Outline each blood parasite and name the species.
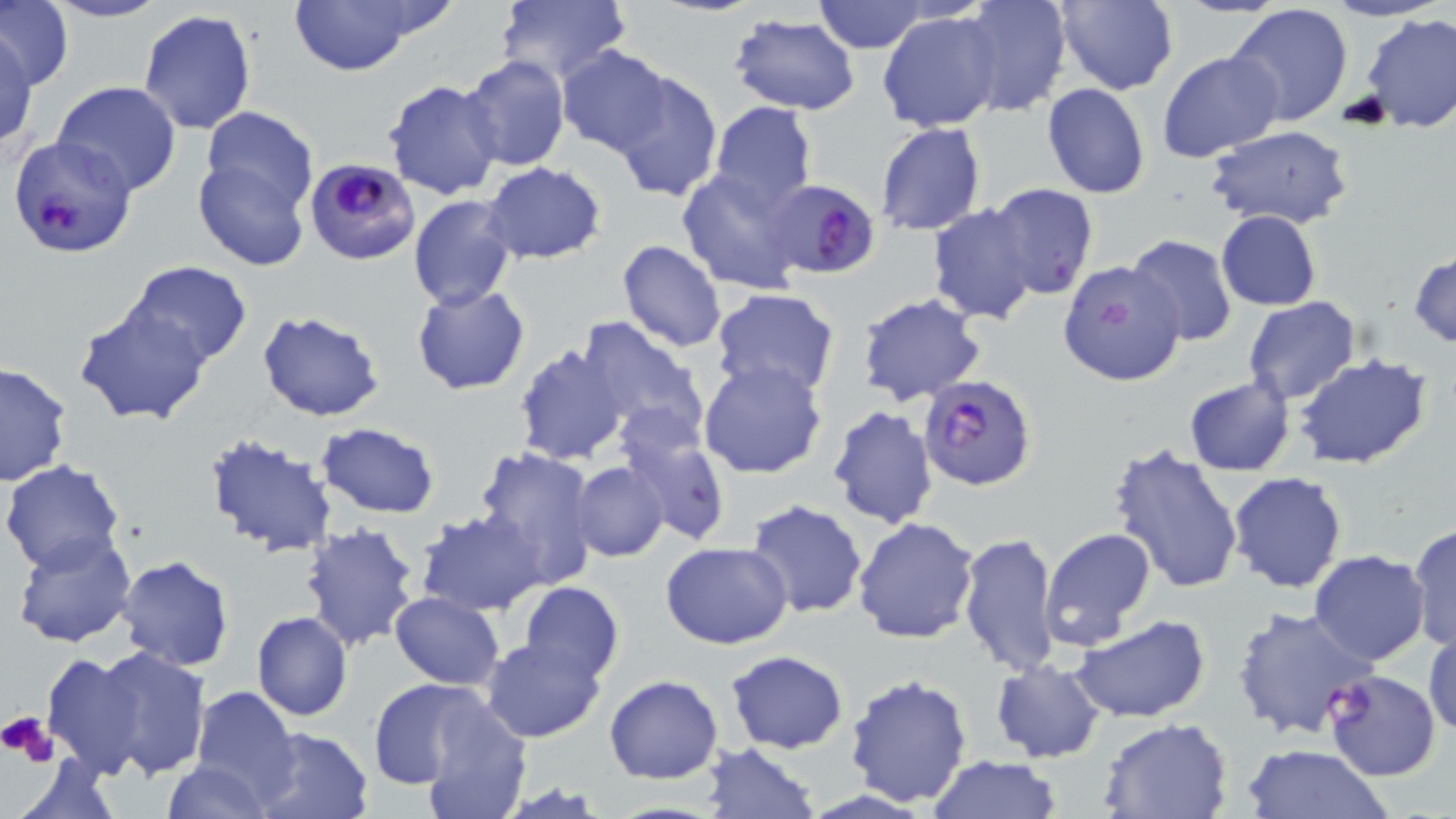

Approximate bounding boxes as (x1, y1, x2, y2) in pixels.
Plasmodium falciparum-infected red blood cells: (8, 135, 136, 259), (304, 158, 421, 266), (766, 178, 880, 278), (916, 375, 1036, 490), (1324, 671, 1439, 781).
No Plasmodium ovale, Plasmodium malariae, Plasmodium vivax, Babesia divergens, or Trypanosoma brucei observed.

Summary:
  - Platelet locations: (1, 711, 58, 766)
  - Uninfected red blood cell locations: (0, 0, 72, 90), (41, 0, 170, 23), (816, 0, 927, 52), (959, 0, 1072, 117), (1053, 0, 1178, 94), (1317, 0, 1446, 22), (289, 1, 434, 76), (495, 1, 631, 89), (1228, 3, 1354, 128), (138, 10, 256, 135), (878, 10, 1003, 132), (728, 13, 861, 114), (1362, 13, 1456, 132), (2, 32, 39, 147), (556, 46, 673, 157), (1158, 50, 1283, 164), (460, 55, 570, 172), (610, 70, 722, 200), (383, 80, 504, 201), (51, 82, 182, 199), (1042, 84, 1149, 199), (709, 102, 818, 214), (198, 107, 319, 221), (874, 123, 987, 236), (1206, 124, 1356, 230), (194, 153, 312, 271), (479, 163, 606, 264), (677, 170, 806, 294), (987, 183, 1099, 301), (407, 195, 518, 310), (928, 203, 1038, 325), (1216, 211, 1321, 310), (1125, 234, 1236, 347), (616, 239, 727, 353), (1409, 253, 1456, 346), (1055, 259, 1184, 388), (125, 261, 252, 369), (412, 286, 530, 395), (710, 288, 840, 402), (855, 292, 985, 408), (1243, 296, 1361, 404), (75, 302, 212, 425), (256, 311, 384, 423), (575, 316, 708, 440), (513, 343, 630, 464), (1292, 353, 1434, 469), (699, 358, 828, 479), (0, 363, 73, 486), (1184, 375, 1295, 476), (826, 406, 938, 530), (619, 416, 732, 548), (315, 423, 440, 518), (204, 431, 337, 559), (1105, 443, 1246, 597), (475, 446, 598, 579), (2, 458, 126, 573), (571, 461, 668, 562), (1226, 471, 1348, 593), (746, 499, 869, 620), (418, 509, 549, 616), (853, 516, 980, 643), (298, 520, 419, 651), (1407, 521, 1455, 653), (1038, 526, 1158, 648), (10, 529, 137, 649), (960, 532, 1060, 677), (661, 541, 794, 649), (1308, 551, 1430, 665), (117, 556, 234, 672), (518, 581, 624, 684), (389, 592, 505, 688), (1229, 606, 1375, 740), (252, 611, 352, 723), (1070, 614, 1211, 723), (1425, 629, 1456, 743), (480, 637, 605, 742), (83, 644, 211, 780), (40, 649, 153, 777), (724, 649, 849, 753), (990, 659, 1107, 764), (604, 673, 724, 784), (843, 674, 972, 807), (366, 677, 492, 790), (190, 685, 299, 799), (415, 696, 535, 819), (1097, 718, 1234, 819), (253, 726, 372, 819), (698, 742, 821, 818), (1241, 742, 1393, 819), (10, 756, 119, 819), (927, 756, 1062, 818), (162, 760, 271, 819)
  - Slide-level diagnosis: Plasmodium falciparum
  - Modality: light microscopy
  - Image size: 1456×819 pixels
  - Field of view: one of a larger specimen
  - Magnification: 1000x
  - Preparation: thin blood film
  - Stain: May-Grünwald-Giemsa